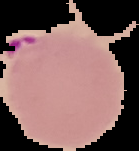
Summary:
  - Result: malaria parasites identified
  - Preparation: thin blood smear
  - Image size: 139×151 pixels
  - Image type: cell region segmented out of the field of view; surrounding area masked to black